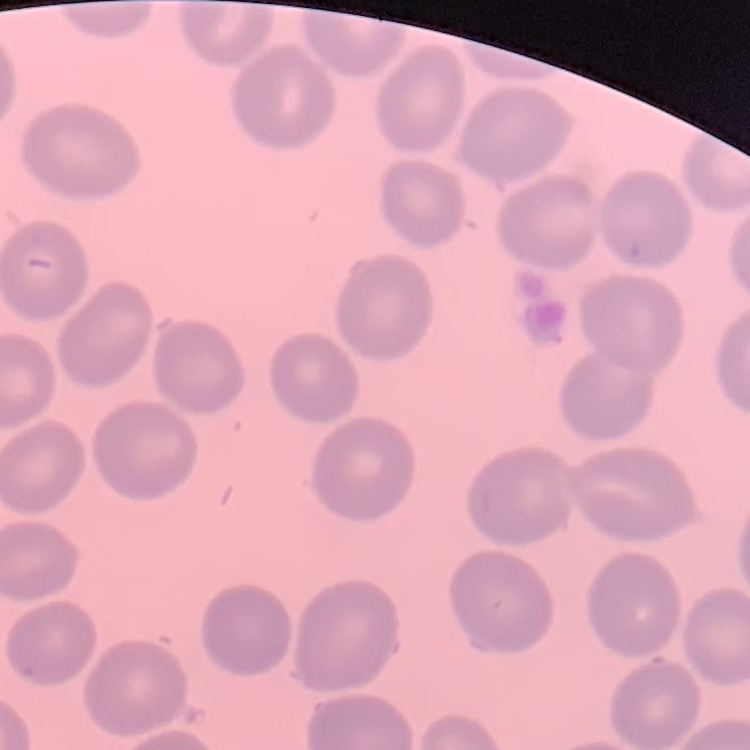
erythrocyte morphology = no rouleaux formation
stain = Field's or Giemsa
preparation = thin blood film
image type = one tile cut from a larger photomicrograph